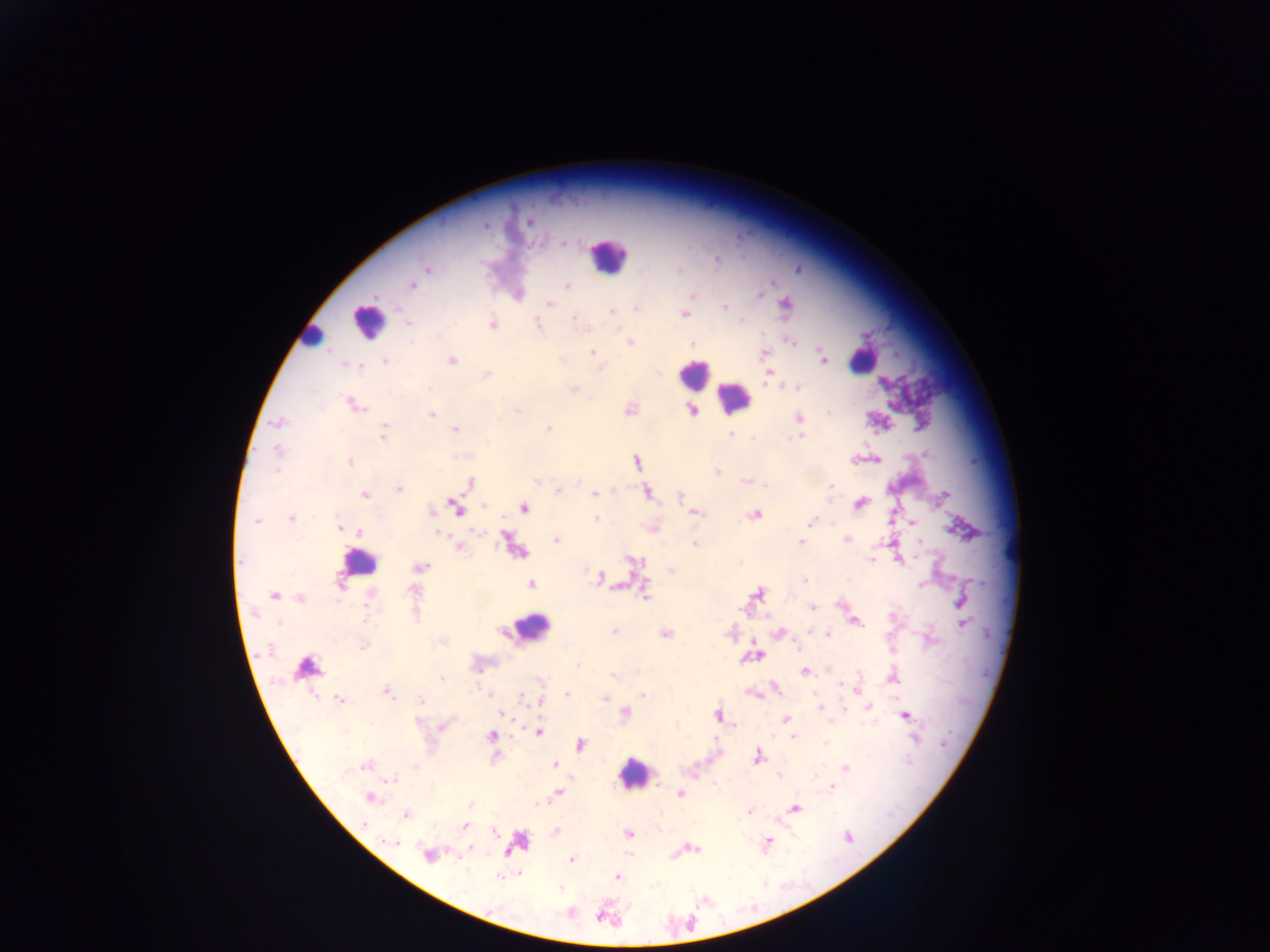
Approximate centers as (x, y) in pixels.
Summary:
  - Leukocyte locations (subset; some below the resolvable size): (607, 255), (366, 322), (311, 338), (862, 359), (693, 375), (734, 396), (359, 561), (530, 628), (633, 772)
  - Plasmodium parasite locations: (529, 221), (486, 224), (562, 243), (717, 260), (426, 269), (679, 270), (412, 285), (567, 286), (693, 294), (761, 294), (550, 302), (786, 304), (723, 307), (636, 309), (613, 310), (685, 314), (574, 317), (742, 320), (537, 322), (409, 324), (493, 325), (790, 341), (629, 342), (692, 343), (592, 352), (764, 353), (822, 357), (452, 360), (385, 362), (356, 366), (601, 367), (487, 375), (768, 378), (430, 387), (797, 387), (574, 388), (354, 405), (517, 410), (629, 410), (692, 411), (431, 414), (799, 418), (279, 421), (455, 429), (548, 429), (384, 432), (731, 433), (799, 436), (752, 437), (487, 442), (277, 452), (877, 459), (350, 461), (636, 462), (718, 472), (746, 481), (470, 483), (765, 485), (830, 485), (398, 490), (558, 491), (594, 493), (647, 493), (945, 494), (364, 495), (679, 497), (861, 503), (483, 505), (455, 508), (524, 509), (432, 511), (697, 513), (754, 515), (290, 518), (596, 518), (257, 522), (811, 522), (913, 523), (339, 528), (359, 532), (478, 532), (440, 533), (846, 540), (556, 541), (801, 541), (919, 542), (695, 544), (460, 547), (871, 560), (634, 561), (421, 567), (671, 570), (600, 578), (804, 580), (340, 583), (531, 584), (921, 584), (412, 590), (757, 593), (646, 595), (274, 596), (301, 598), (960, 600), (812, 607), (367, 618), (280, 621), (856, 622), (964, 623), (809, 631), (615, 632), (780, 633), (665, 634), (827, 635), (363, 646), (756, 655), (578, 665), (306, 667), (807, 672), (612, 675), (442, 679), (839, 684), (776, 689), (856, 690), (387, 692), (489, 694), (567, 694), (643, 695), (521, 697), (606, 697), (339, 700), (422, 700), (540, 701), (870, 707), (820, 708), (502, 714), (624, 714), (717, 715), (906, 716), (786, 719), (418, 721), (443, 725), (346, 732), (540, 732), (491, 736), (793, 737), (825, 743), (581, 744), (757, 756), (555, 764), (365, 765), (845, 768), (778, 776), (815, 776), (392, 780), (832, 787), (558, 793), (681, 794), (370, 797), (470, 804), (795, 808), (749, 811), (406, 816), (465, 826), (628, 833), (847, 836), (390, 841), (768, 842), (693, 848), (470, 850), (428, 855), (572, 860), (502, 877), (617, 877)
  - Country: Ghana
  - Image size: 1270×952 pixels
  - Preparation: thick blood smear
  - Field of view: single
  - Capture: mobile-phone photograph through a microscope